Give the position of every Plasmodium parasite visible.
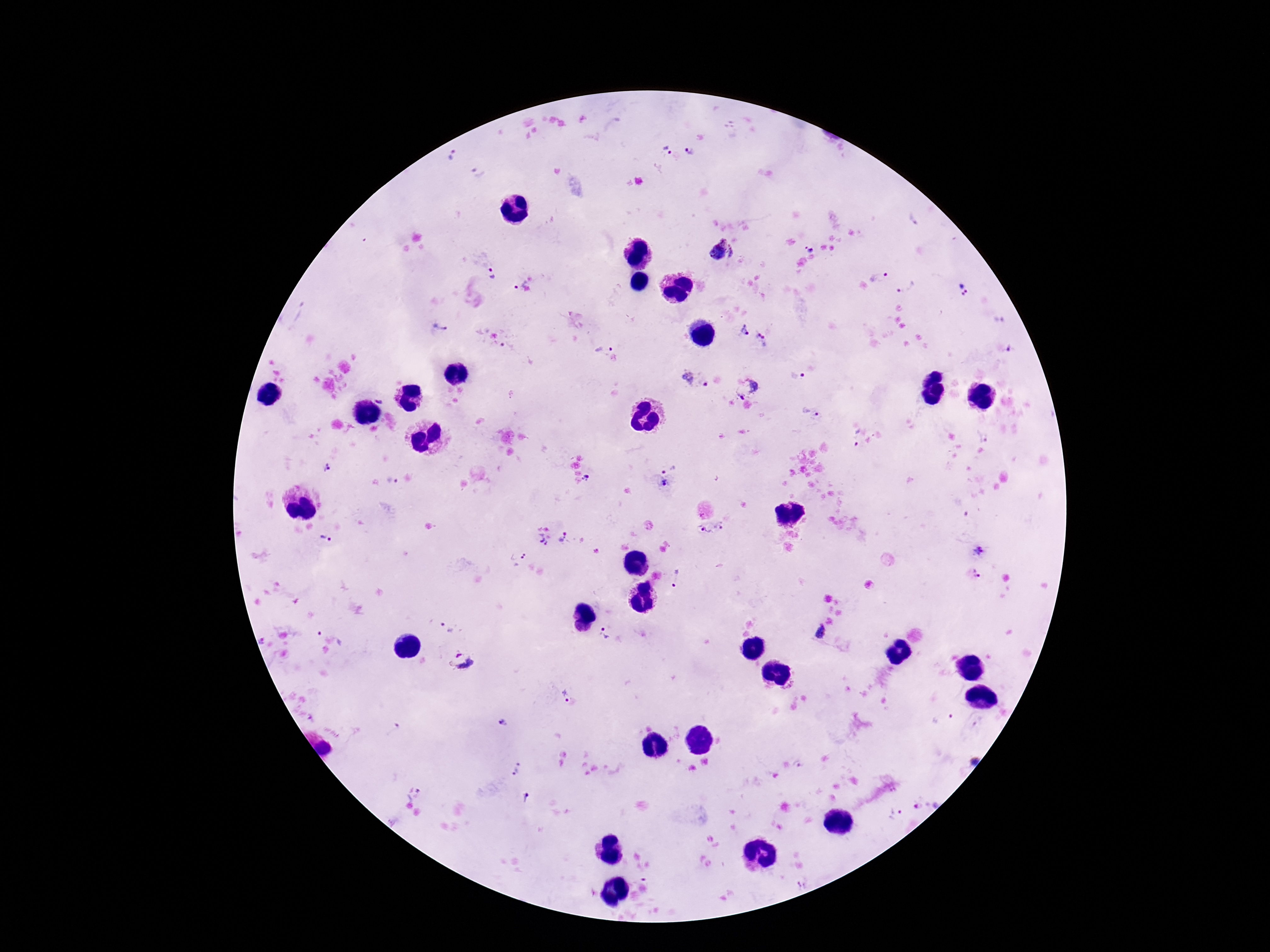

Approximate object centers, in pixels from the top-left corner.
Plasmodium parasites: (x=666, y=150), (x=689, y=151), (x=453, y=157), (x=479, y=173), (x=809, y=249), (x=722, y=251), (x=492, y=274), (x=877, y=275), (x=519, y=283), (x=906, y=285), (x=962, y=289), (x=1000, y=320), (x=439, y=329), (x=745, y=331), (x=762, y=338), (x=599, y=347), (x=796, y=375), (x=695, y=380), (x=747, y=389), (x=380, y=398), (x=812, y=409), (x=856, y=436), (x=668, y=467), (x=328, y=468), (x=586, y=479), (x=391, y=480), (x=665, y=483), (x=720, y=525), (x=706, y=532), (x=552, y=536), (x=326, y=538), (x=978, y=551), (x=524, y=556), (x=976, y=573), (x=678, y=579), (x=446, y=626), (x=331, y=633), (x=819, y=633), (x=605, y=634), (x=461, y=662), (x=566, y=695), (x=945, y=719), (x=500, y=721), (x=973, y=760), (x=516, y=769), (x=527, y=798), (x=926, y=806), (x=894, y=812).

{
  "patient_malaria_status": "infected",
  "image_size": "1270×952 pixels",
  "capture": "smartphone camera through the microscope eyepiece",
  "stain": "Giemsa",
  "magnification": "100x",
  "field_of_view": "single",
  "preparation": "thick blood smear"
}